Identify the cell.
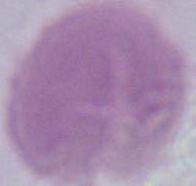

An erythrocyte.

Summary:
  - Magnification: 1000x
  - Modality: photomicrograph